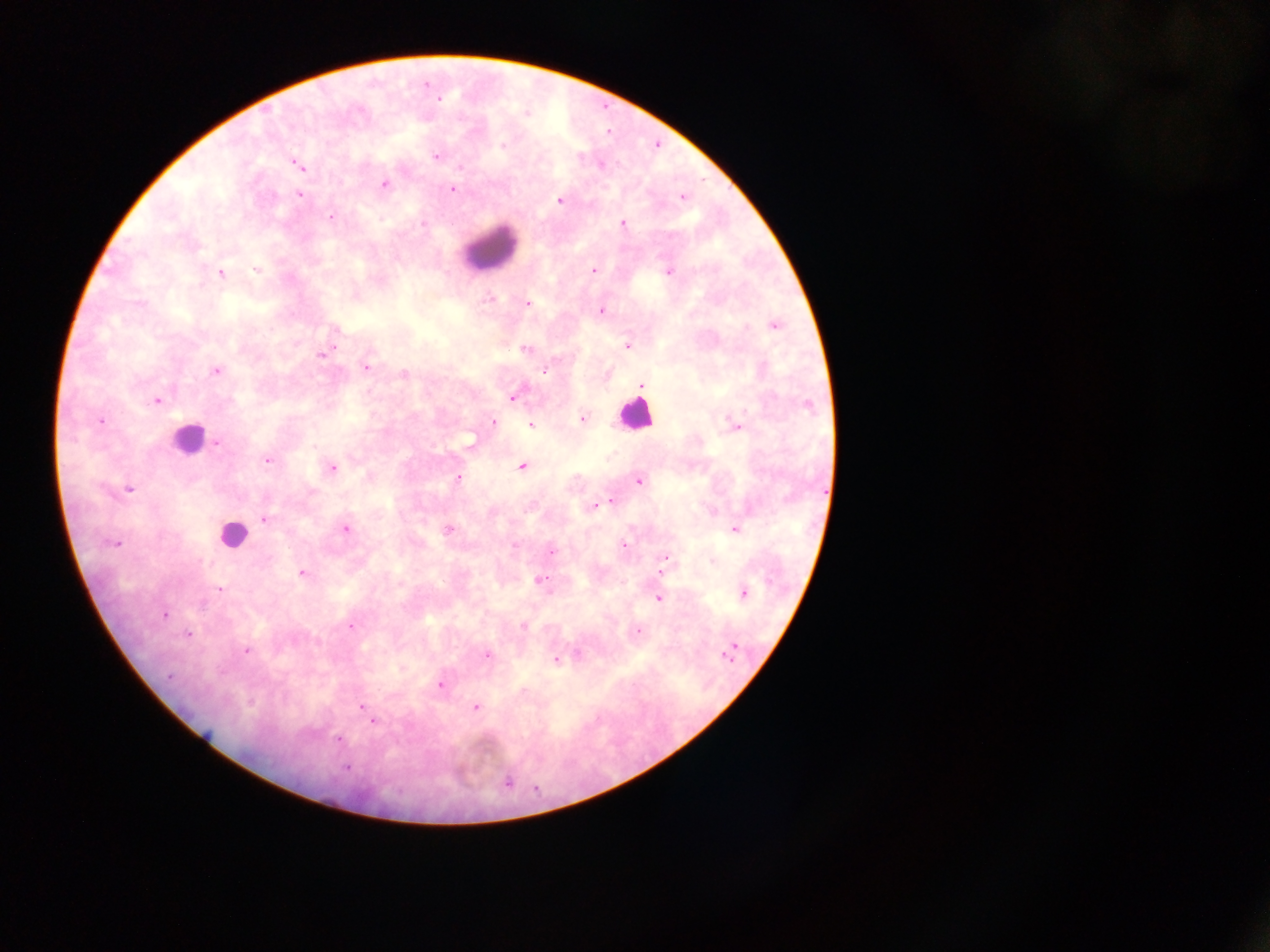

Approximate centers as x y in pixels.
Summary:
  - Plasmodium parasite locations: 440 99; 503 144; 436 156; 297 164; 601 165; 459 166; 384 183; 452 189; 299 194; 682 197; 560 200; 331 217; 422 224; 623 224; 256 270; 593 270; 668 272; 220 273; 487 299; 527 303; 601 311; 775 326; 627 346; 525 349; 321 355; 366 367; 216 371; 545 371; 404 374; 642 385; 513 397; 156 401; 809 406; 582 418; 100 421; 493 422; 531 426; 735 426; 218 443; 268 460; 522 466; 332 468; 459 478; 639 481; 130 489; 610 502; 593 506; 265 519; 345 529; 735 529; 448 531; 114 543; 624 545; 551 551; 664 559; 662 570; 302 574; 540 580; 220 589; 743 593; 659 598; 164 615; 524 626; 351 627; 638 632; 188 634; 734 646; 246 650; 487 655; 727 656; 556 660; 169 675; 441 684; 361 706; 476 707; 373 721; 338 739; 347 768; 508 782
  - Leukocyte locations: 488 249; 634 414; 187 440; 232 534
  - Capture: mobile-phone photograph through a microscope
  - Country: Ghana
  - Preparation: thick blood smear
  - Field of view: single
  - Image size: 1270×952 pixels